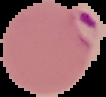

Summary:
  - Preparation: thin blood smear
  - Malaria status: parasitized
  - Image type: cell region segmented out of the field of view; surrounding area masked to black
  - Image size: 106×97 pixels